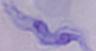

A trypanosome is seen. 1000x magnification. Photomicrograph.